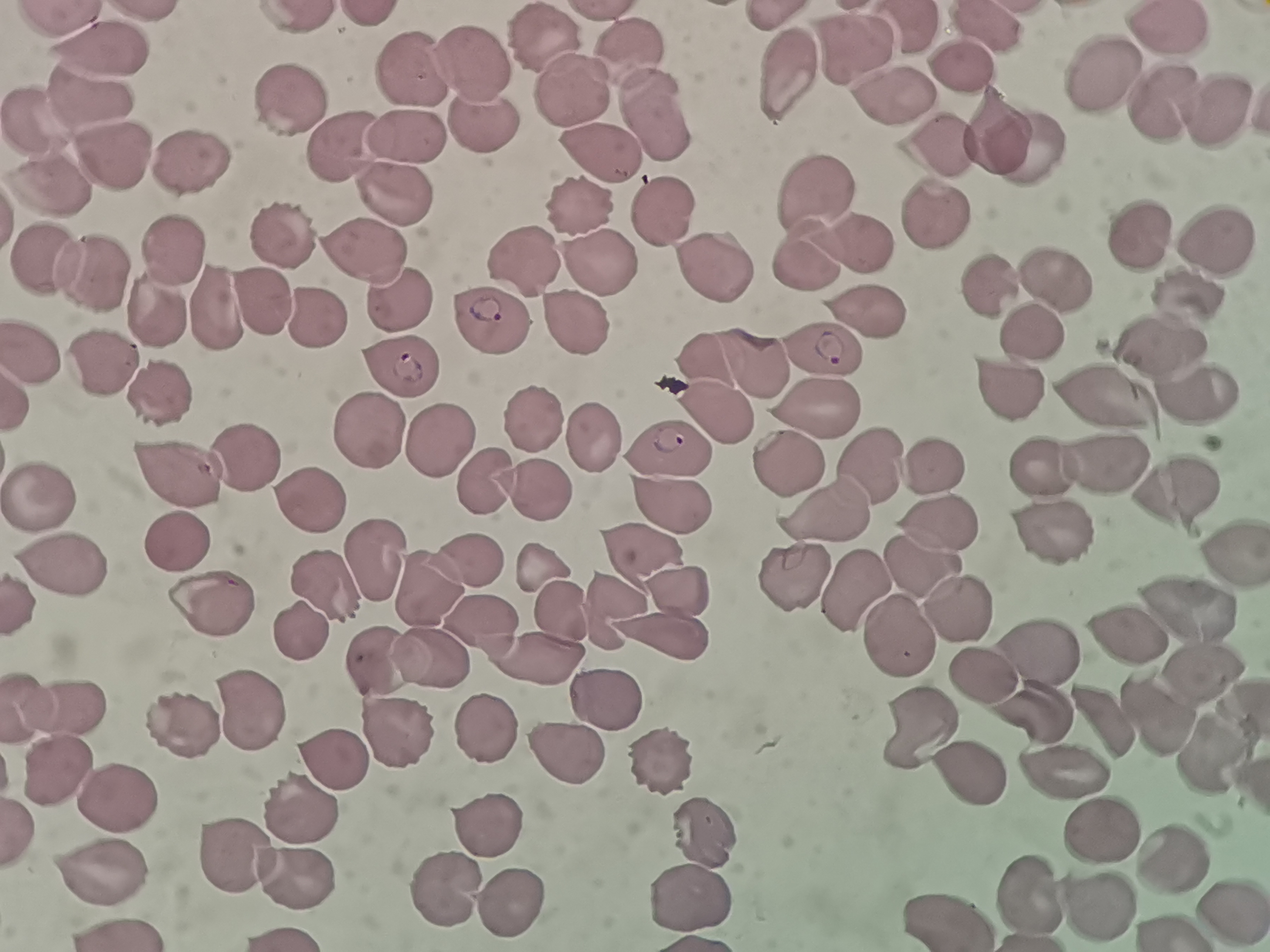

cell locations = approximate centers as [x, y] in pixels: [1162, 29], [548, 34], [855, 45], [100, 52], [634, 55], [470, 60], [961, 65], [1103, 74], [410, 75], [787, 79], [575, 87], [87, 96], [1162, 99], [284, 100], [897, 100], [656, 112], [1215, 112], [46, 116], [487, 129], [1001, 129], [406, 138], [1027, 143], [936, 145], [596, 148], [347, 149], [195, 159], [112, 161], [819, 186], [53, 189], [399, 196], [939, 208], [578, 212], [656, 212], [1134, 235], [283, 236], [1216, 240], [861, 247], [172, 251], [366, 251], [802, 257], [527, 261], [96, 267], [709, 269], [599, 273], [1056, 277], [991, 289], [1193, 294], [268, 302], [218, 308], [407, 308], [157, 309], [319, 313], [576, 322], [497, 325], [1035, 333], [826, 344], [1163, 345], [36, 352], [754, 354], [113, 356], [702, 358], [401, 367], [1011, 385], [1105, 393], [1205, 395], [818, 402], [713, 413], [532, 417], [367, 428], [595, 431], [440, 440], [670, 450], [247, 458], [789, 458], [1112, 460], [868, 463], [932, 463], [1044, 465], [184, 473], [490, 483], [1180, 486], [537, 488], [43, 497], [316, 502], [674, 507], [825, 510], [945, 515], [1048, 520], [183, 537], [1234, 540], [632, 546], [478, 557], [372, 560], [66, 561], [921, 561], [542, 564], [326, 582], [852, 587], [433, 589], [677, 589], [215, 600], [1187, 603], [557, 604], [959, 609], [484, 623], [304, 630], [1129, 631], [898, 635], [664, 640], [1039, 646], [535, 656], [388, 658], [439, 665], [983, 670], [1209, 675], [607, 699], [70, 711], [1037, 711], [248, 713], [1153, 713], [190, 719], [486, 722], [1104, 724], [401, 731], [925, 733], [565, 751], [1219, 754], [651, 759], [66, 769], [335, 771], [976, 772], [1069, 775], [116, 799], [302, 802], [488, 821], [709, 829], [1105, 831], [239, 853], [1174, 858], [114, 872], [296, 873], [445, 883], [696, 892], [1028, 894], [503, 905], [1098, 907], [1236, 909], [953, 917]
stain = Giemsa
field of view = single
preparation = thin blood smear
capture = smartphone through the microscope eyepiece
image size = 1270×952 pixels